Identify the parasite.
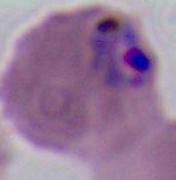
Plasmodium.

Captured at either 400x or 1000x magnification. Micrograph.